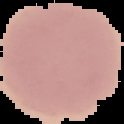
Summary:
  - Image size: 124×124 pixels
  - Image type: segmented cell region on a black background
  - Malaria status: uninfected
  - Preparation: thin blood smear